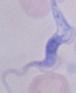 Micrograph. 1000x magnification. A trypanosome is shown.